Describe the morphology of the erythrocytes.
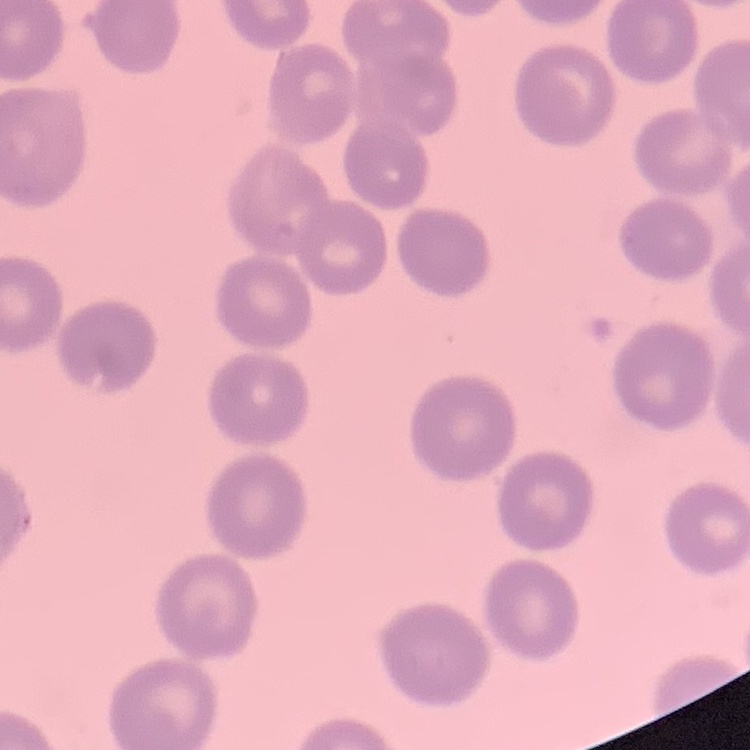

They show no rouleaux formation.

image type = one tile cut from a larger photomicrograph
preparation = thin peripheral smear
stain = Field's or Giemsa